Give the extent of all Plasmodium ovale-infected red blood cells.
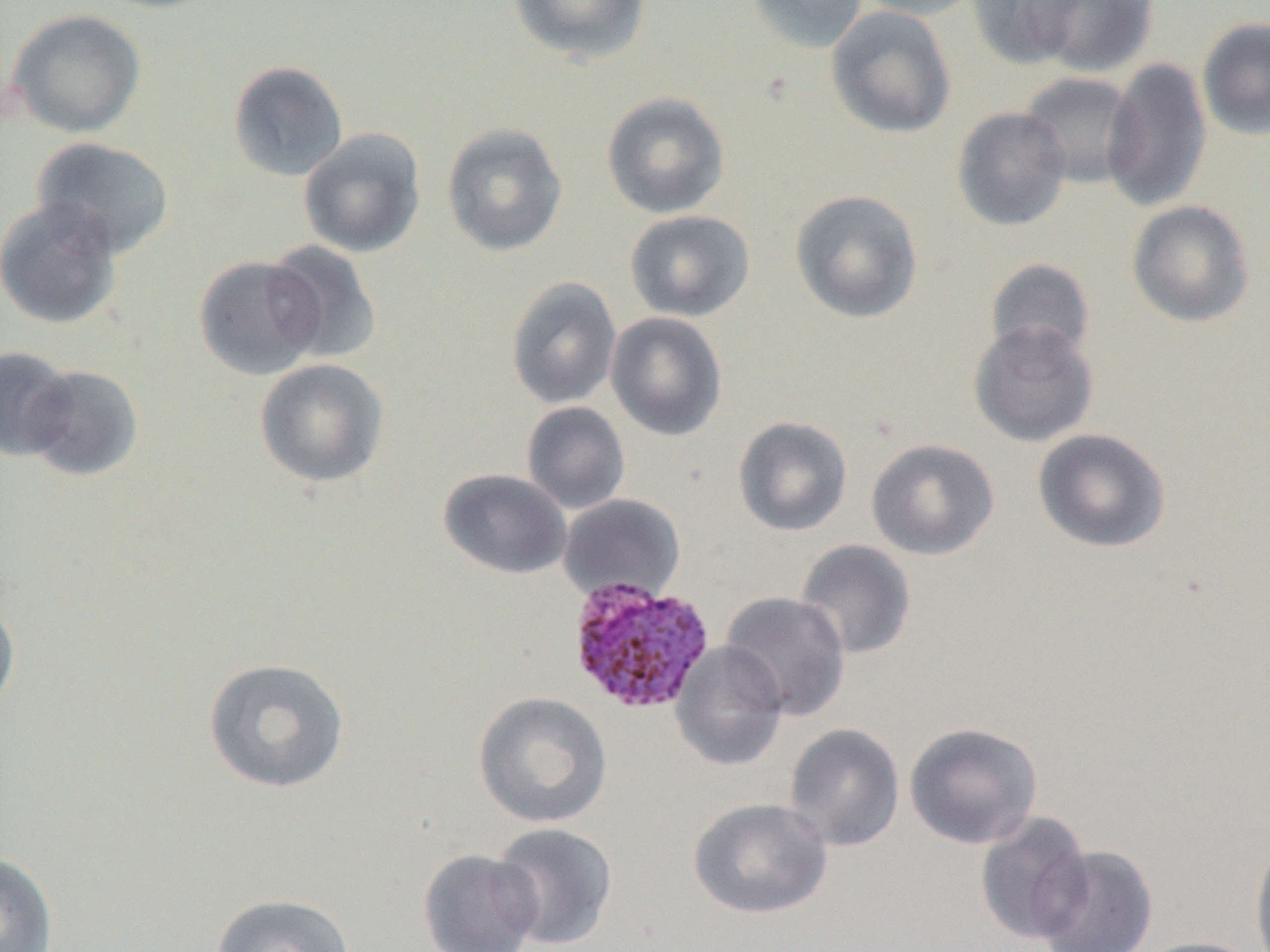
Approximate bounding boxes as (x1,y1)-(x2,y2) corner pairs in pixels.
Plasmodium ovale-infected red blood cells: (567,576)-(715,716).

Uninfected red blood cell locations: (508,0)-(652,66), (747,0)-(869,54), (855,0)-(983,20), (967,0)-(1088,69), (1031,0)-(1158,77), (826,6)-(957,140), (6,9)-(147,138), (1197,16)-(1270,141), (1102,57)-(1212,213), (228,61)-(349,182), (1018,71)-(1142,189), (601,91)-(731,219), (952,106)-(1072,232), (441,122)-(569,257), (298,128)-(427,258), (31,137)-(176,259), (790,189)-(924,323), (0,196)-(124,329), (1126,200)-(1255,328), (625,210)-(755,322), (264,241)-(383,364), (193,254)-(325,381), (985,259)-(1096,363), (505,277)-(622,410), (605,311)-(727,441), (968,321)-(1099,447), (0,346)-(76,461), (254,358)-(389,488), (22,364)-(145,481), (522,401)-(630,514), (733,416)-(852,537), (1032,428)-(1171,553), (865,438)-(999,560), (438,468)-(572,580), (558,494)-(686,603), (794,539)-(916,660), (720,591)-(851,721), (0,594)-(21,720), (670,640)-(789,771), (202,657)-(350,794), (473,692)-(612,827), (904,721)-(1043,850), (784,723)-(905,852), (688,797)-(832,919), (974,810)-(1093,945), (490,822)-(618,950), (1250,834)-(1270,952), (1034,844)-(1158,952), (418,849)-(543,952), (0,851)-(59,952), (210,893)-(356,952), (1131,936)-(1266,952). Slide-level diagnosis: Plasmodium ovale. Optical microscopy. Thin blood smear. One field of a larger specimen. Image is 1270×952 pixels. Captured at 1000x magnification.